Identify the blood parasite species.
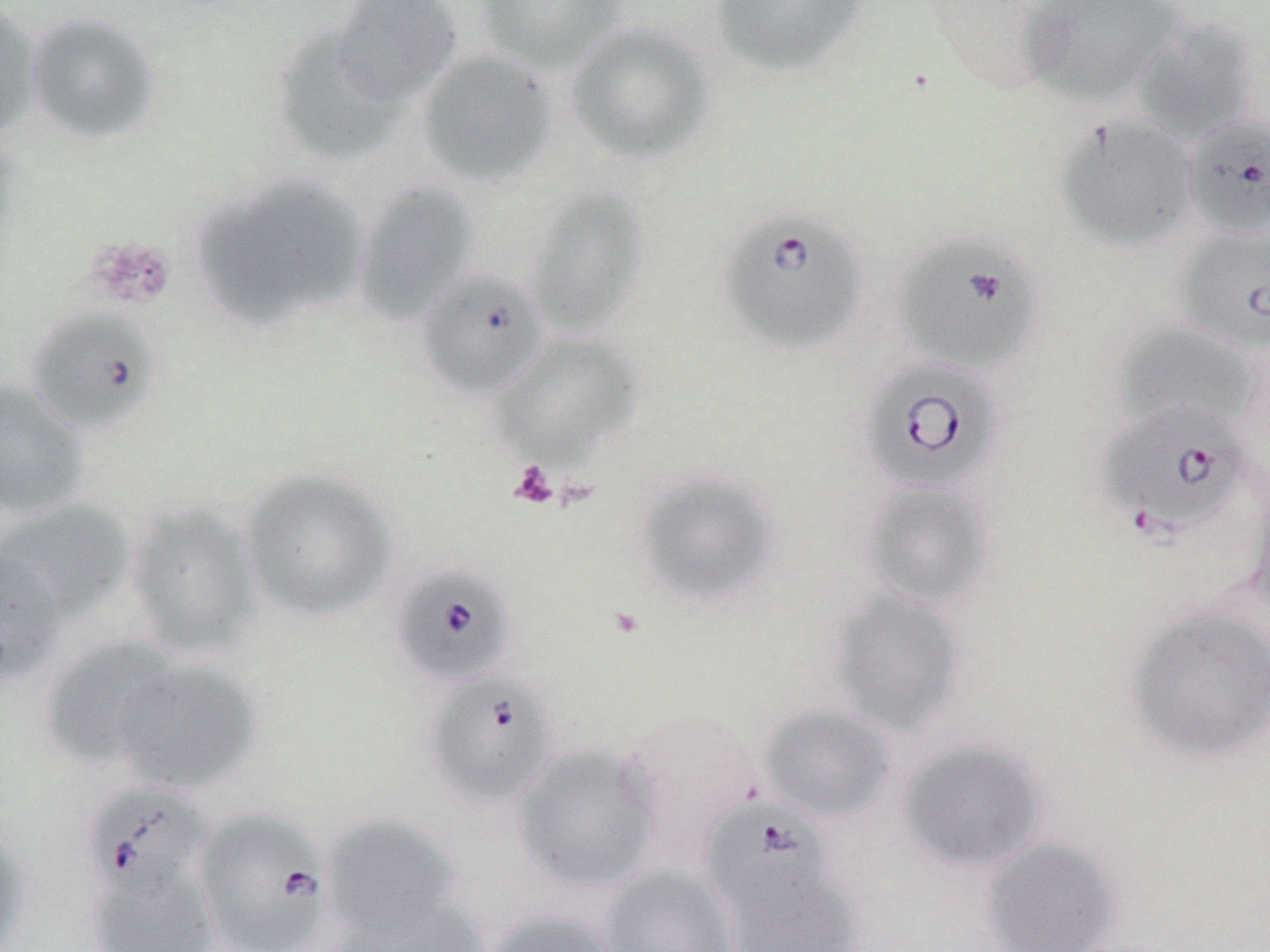
Babesia divergens.

{
  "platelet_locations": "approximate bounding boxes as named x1/y1/x2/y2 corners in pixels: (x1=85, y1=235, x2=176, y2=310), (x1=508, y1=461, x2=559, y2=509)",
  "magnification": "1000x",
  "uninfected_red_blood_cell_locations": "approximate bounding boxes as named x1/y1/x2/y2 corners in pixels: (x1=330, y1=0, x2=463, y2=106), (x1=474, y1=0, x2=629, y2=73), (x1=709, y1=0, x2=870, y2=78), (x1=1017, y1=0, x2=1187, y2=109), (x1=0, y1=2, x2=44, y2=141), (x1=23, y1=10, x2=164, y2=147), (x1=1131, y1=16, x2=1261, y2=145), (x1=565, y1=21, x2=716, y2=165), (x1=269, y1=22, x2=405, y2=167), (x1=415, y1=48, x2=558, y2=188), (x1=1053, y1=114, x2=1199, y2=252), (x1=238, y1=175, x2=370, y2=315), (x1=354, y1=180, x2=481, y2=323), (x1=524, y1=185, x2=649, y2=338), (x1=190, y1=192, x2=320, y2=331), (x1=1112, y1=321, x2=1262, y2=437), (x1=491, y1=332, x2=644, y2=468), (x1=0, y1=379, x2=91, y2=521), (x1=238, y1=466, x2=397, y2=624), (x1=632, y1=468, x2=782, y2=610), (x1=1247, y1=476, x2=1270, y2=622), (x1=861, y1=479, x2=995, y2=610), (x1=121, y1=499, x2=265, y2=661), (x1=1, y1=500, x2=138, y2=628), (x1=0, y1=545, x2=63, y2=686), (x1=826, y1=588, x2=968, y2=736), (x1=1124, y1=603, x2=1270, y2=766), (x1=38, y1=635, x2=182, y2=771), (x1=112, y1=658, x2=262, y2=795), (x1=758, y1=703, x2=895, y2=823), (x1=617, y1=707, x2=764, y2=863), (x1=898, y1=740, x2=1048, y2=874), (x1=511, y1=743, x2=660, y2=892), (x1=320, y1=813, x2=463, y2=945), (x1=0, y1=818, x2=33, y2=952), (x1=981, y1=836, x2=1123, y2=952), (x1=720, y1=859, x2=865, y2=952), (x1=83, y1=863, x2=221, y2=951), (x1=598, y1=864, x2=740, y2=952), (x1=334, y1=897, x2=493, y2=952), (x1=481, y1=908, x2=623, y2=952)",
  "stain": "May-Grünwald-Giemsa",
  "modality": "light microscopy",
  "field_of_view": "one of a larger specimen",
  "babesia_divergens_infected_red_blood_cell_locations": "approximate bounding boxes as named x1/y1/x2/y2 corners in pixels: (x1=1183, y1=113, x2=1270, y2=240), (x1=717, y1=206, x2=869, y2=356), (x1=1175, y1=225, x2=1270, y2=353), (x1=892, y1=231, x2=1043, y2=376), (x1=415, y1=266, x2=550, y2=400), (x1=23, y1=306, x2=163, y2=435), (x1=860, y1=356, x2=1006, y2=496), (x1=1098, y1=402, x2=1255, y2=539), (x1=391, y1=562, x2=517, y2=687), (x1=423, y1=672, x2=560, y2=810), (x1=82, y1=782, x2=216, y2=903), (x1=700, y1=798, x2=840, y2=922), (x1=192, y1=807, x2=334, y2=952)",
  "image_size": "1270×952 pixels",
  "preparation": "thin blood film"
}